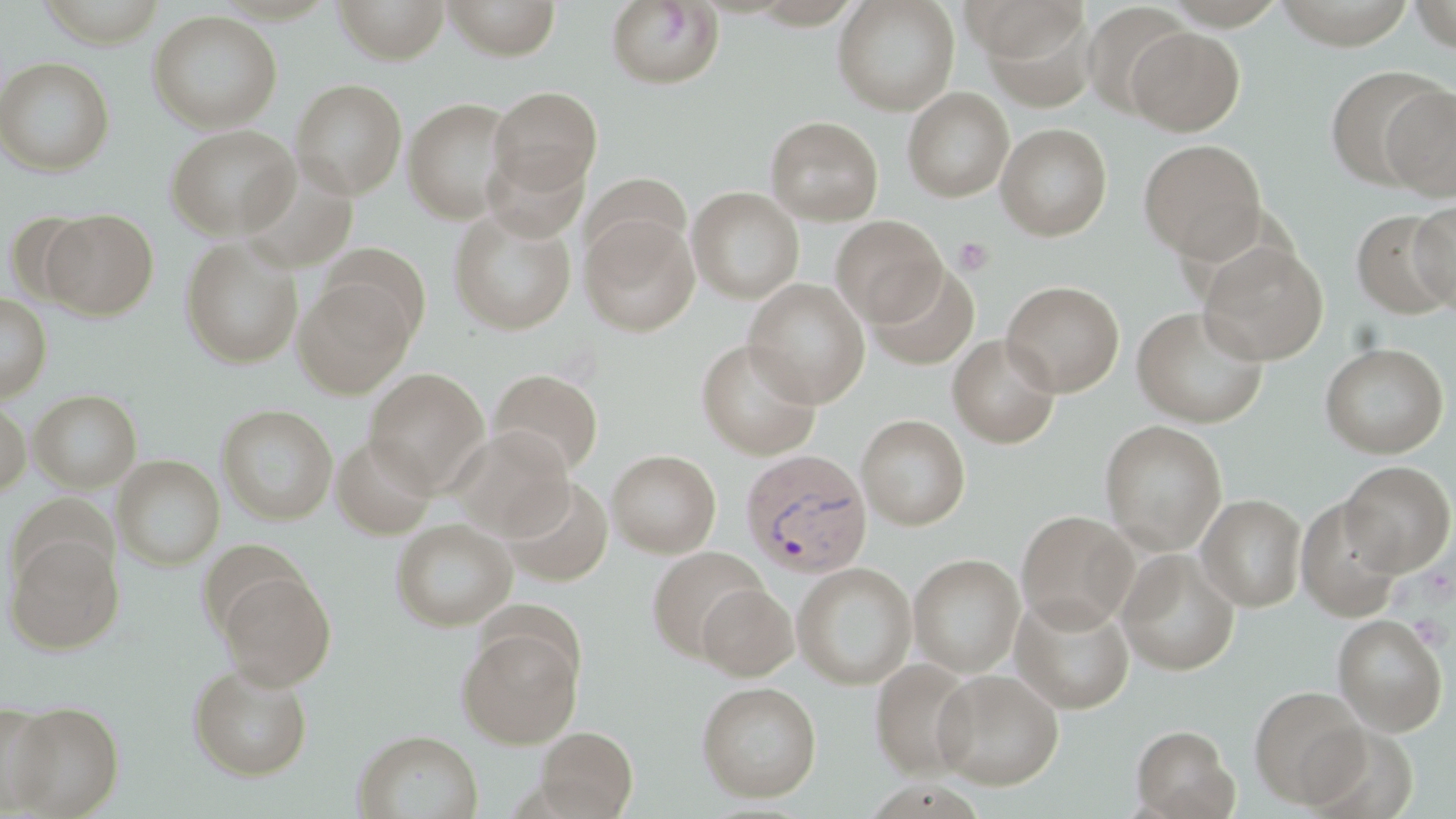 Approximate bounding boxes as (x1,y1)-(x2,y2) corner pairs in pixels. Uninfected red blood cell locations: (334,0)-(450,64), (443,0)-(560,60), (832,0)-(960,115), (1407,0)-(1456,52), (606,1)-(725,89), (975,1)-(1097,107), (1080,2)-(1191,118), (147,10)-(283,133), (1127,27)-(1245,136), (0,56)-(115,176), (1323,64)-(1452,191), (290,78)-(408,199), (1382,84)-(1456,201), (488,86)-(603,197), (902,87)-(1014,202), (403,97)-(518,223), (765,116)-(884,225), (995,122)-(1112,241), (165,124)-(300,239), (1138,139)-(1267,262), (483,148)-(590,242), (580,173)-(692,270), (583,177)-(788,283), (687,186)-(804,304), (1410,199)-(1456,315), (448,205)-(577,335), (40,208)-(158,320), (5,210)-(98,307), (1351,210)-(1455,318), (580,214)-(700,336), (832,215)-(946,326), (180,235)-(303,369), (1197,239)-(1329,364), (314,245)-(432,345), (868,263)-(979,370), (294,275)-(417,398), (744,279)-(870,407), (1001,280)-(1125,397), (0,293)-(51,402), (1132,306)-(1269,428), (948,334)-(1061,448), (696,338)-(822,459), (1319,342)-(1449,459), (364,368)-(491,496), (488,368)-(605,478), (29,389)-(142,493), (0,397)-(31,498), (217,404)-(338,524), (856,414)-(970,530), (1098,419)-(1228,555), (450,427)-(574,542), (331,433)-(437,539), (607,449)-(721,557), (113,455)-(225,571), (1339,460)-(1455,576), (502,478)-(613,586), (1197,493)-(1308,611), (1295,497)-(1404,620), (1016,509)-(1138,632), (390,518)-(518,631), (6,534)-(123,653), (646,546)-(768,662), (1117,549)-(1240,676), (908,553)-(1026,678), (792,561)-(917,690), (216,568)-(336,689), (696,582)-(798,681), (1012,593)-(1134,713), (1332,614)-(1448,736), (457,622)-(583,748), (871,658)-(978,779), (188,663)-(313,780), (932,669)-(1064,789), (696,680)-(822,802), (1248,685)-(1371,808), (6,701)-(124,817), (0,703)-(58,813), (1131,724)-(1239,819), (535,726)-(638,818), (353,729)-(484,819). Plasmodium vivax-infected red blood cell locations: (740,448)-(874,579). Platelet locations: (953,236)-(996,277), (1419,565)-(1455,604). Slide-level diagnosis: Plasmodium vivax. 1000x magnification. One field of a larger specimen. Image is 1456×819 pixels. May-Grünwald-Giemsa stain. Thin blood smear. Optical microscopy.